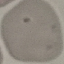

Malaria status: uninfected. Cell patch, automatically extracted from a larger field of view and resized to 64 × 64 pixels. Acquired by smartphone through the microscope eyepiece. Thin smear of blood. Giemsa-stained preparation.